Classify this cell by malaria status.
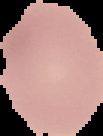

Uninfected.

Cell region segmented out of the field of view; the surrounding area is masked to black. Image is 103×136 pixels. From a thin blood film.